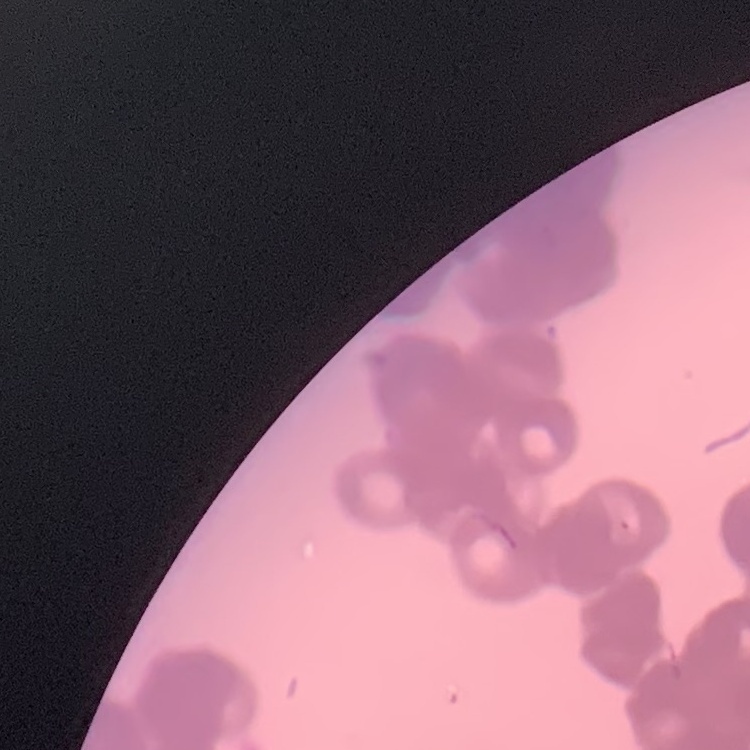
Summary:
  - Red blood cell morphology: rouleaux formation
  - Preparation: thin peripheral smear
  - Stain: Field's or Giemsa
  - Image type: square crop of a larger photomicrograph